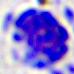

Summary:
  - Magnification: 400x
  - Identification: white blood cell
  - Modality: photomicrograph